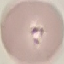

result = malaria parasites detected
capture = smartphone camera at the microscope eyepiece
stain = Giemsa
preparation = thin blood smear
image type = automatically extracted cell patch, resized to 64 × 64 pixels